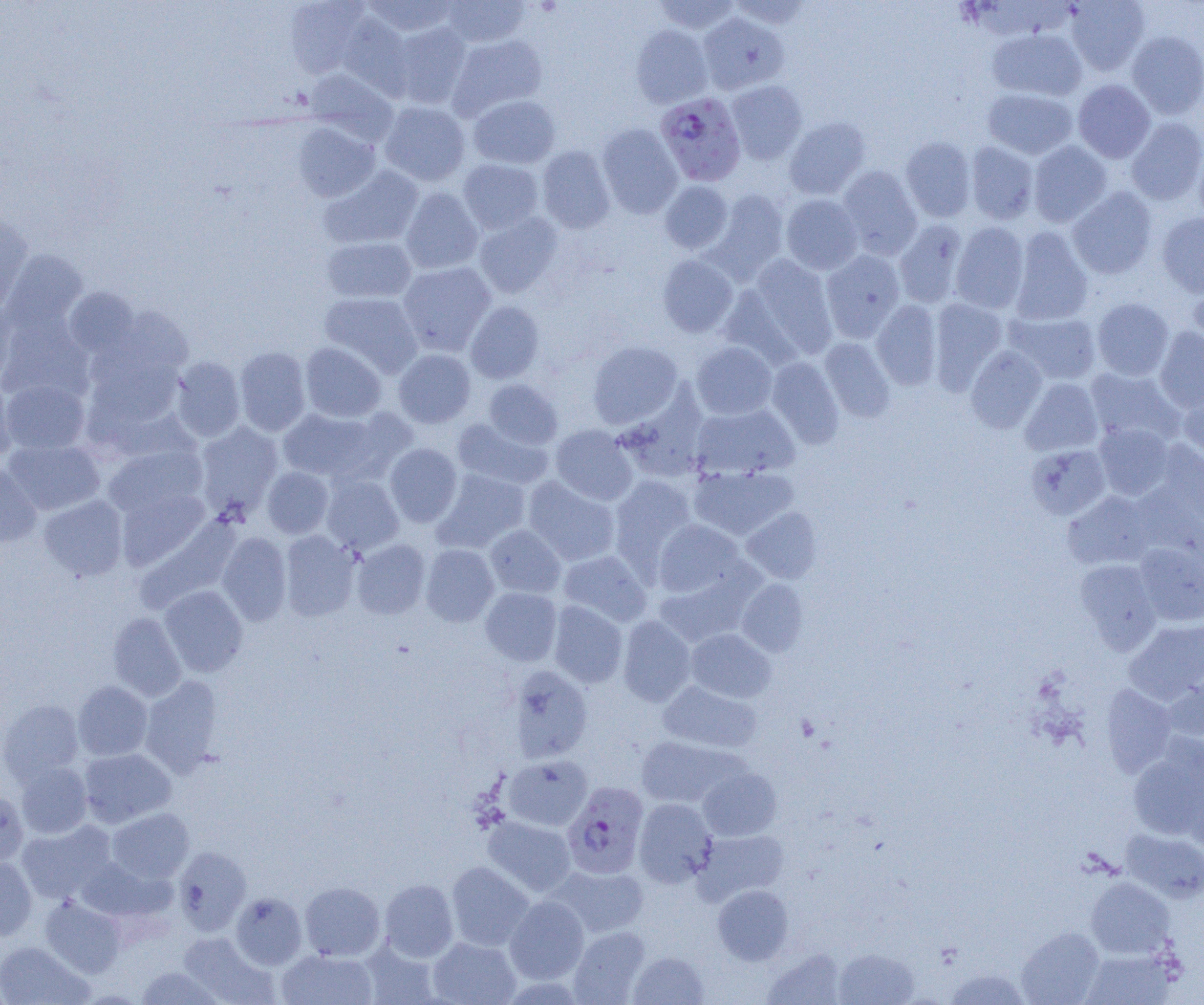

slide-level diagnosis = Plasmodium falciparum
modality = optical microscopy
Plasmodium falciparum-infected red blood cell locations = approximate bounding boxes as (x1,y1)-(x2,y2) corner pairs in pixels: (655,92)-(746,186), (562,782)-(649,879)
uninfected red blood cell locations = approximate bounding boxes as (x1,y1)-(x2,y2) corner pairs in pixels: (284,0)-(374,79), (361,0)-(460,37), (441,0)-(531,48), (653,0)-(740,34), (728,0)-(812,29), (1065,0)-(1150,75), (698,12)-(788,93), (336,13)-(414,98), (389,22)-(472,108), (631,25)-(713,108), (987,28)-(1087,101), (1127,30)-(1204,118), (447,34)-(547,120), (304,68)-(398,143), (726,80)-(807,164), (1073,80)-(1155,163), (982,87)-(1077,159), (469,95)-(561,169), (379,101)-(470,186), (292,112)-(471,191), (784,117)-(871,199), (1126,117)-(1204,205), (292,121)-(380,202), (597,124)-(682,218), (901,136)-(976,222), (966,141)-(1038,224), (1028,141)-(1112,227), (536,145)-(616,233), (1193,147)-(1204,227), (458,158)-(543,234), (319,166)-(424,250), (837,166)-(922,259), (659,181)-(733,254), (400,187)-(483,274), (1068,187)-(1157,279), (706,190)-(789,281), (781,194)-(863,274), (474,212)-(563,298), (1157,212)-(1204,298), (0,215)-(34,316), (895,219)-(968,308), (950,223)-(1029,313), (1010,228)-(1092,325), (322,236)-(417,303), (3,249)-(87,331), (820,250)-(905,341), (657,254)-(738,337), (744,256)-(838,359), (397,261)-(495,355), (1186,284)-(1204,354), (64,287)-(142,360), (320,292)-(423,377), (1092,298)-(1174,380), (929,299)-(1007,392), (872,300)-(942,389), (465,301)-(545,383), (0,302)-(18,388), (108,305)-(194,378), (1006,310)-(1101,384), (0,314)-(95,403), (1154,326)-(1204,412), (819,337)-(895,422), (588,341)-(682,428), (691,342)-(778,420), (300,343)-(386,422), (965,346)-(1046,433), (234,347)-(311,436), (85,349)-(186,432), (393,349)-(476,428), (170,357)-(245,442), (766,358)-(844,448), (1085,368)-(1184,447), (1020,378)-(1103,456), (1,379)-(90,454), (484,379)-(563,449), (0,380)-(17,462), (1178,386)-(1204,463), (616,390)-(712,483), (690,403)-(800,480), (278,407)-(382,483), (452,418)-(553,490), (195,421)-(283,517), (1094,423)-(1174,500), (551,425)-(637,505), (3,440)-(104,515), (1156,440)-(1204,521), (384,443)-(462,527), (1026,444)-(1111,520), (103,445)-(207,520), (0,462)-(41,548), (689,464)-(798,540), (262,467)-(333,538), (433,469)-(530,552), (322,475)-(403,555), (609,475)-(698,573), (523,477)-(620,566), (115,488)-(209,571), (1063,492)-(1156,570), (39,495)-(128,581), (741,507)-(822,583), (136,516)-(242,613), (653,519)-(747,599), (485,524)-(566,598), (279,530)-(360,621), (217,532)-(291,626), (351,539)-(431,619), (1134,542)-(1204,625), (420,544)-(499,626), (559,550)-(651,626), (1075,559)-(1161,653), (736,578)-(808,656), (159,585)-(248,677), (480,587)-(562,666), (548,601)-(628,688), (108,612)-(187,701), (618,615)-(696,707), (1125,619)-(1204,704), (685,629)-(776,703), (507,665)-(593,763), (1162,671)-(1204,743), (139,675)-(224,777), (73,681)-(152,761), (658,681)-(761,753), (1101,685)-(1177,776), (0,698)-(84,784), (635,736)-(743,808), (1128,739)-(1204,841), (79,748)-(176,827), (503,755)-(593,831), (16,762)-(92,839), (698,767)-(781,841), (0,791)-(29,868), (634,798)-(717,887), (107,808)-(194,883), (482,816)-(576,897), (17,820)-(116,904), (694,828)-(789,904), (1121,828)-(1204,903), (173,846)-(251,935), (0,857)-(37,941), (75,857)-(174,926), (446,861)-(535,951), (550,864)-(650,937), (1086,877)-(1174,958), (379,879)-(458,962), (300,881)-(385,961), (713,884)-(793,965), (231,892)-(306,969), (505,895)-(589,984), (40,896)-(126,977), (568,926)-(651,1004), (1016,927)-(1104,1005), (177,932)-(278,1004), (427,936)-(521,1005), (359,940)-(441,1005), (0,941)-(92,1005), (833,947)-(919,1005), (1080,948)-(1178,1005), (276,949)-(378,1005), (761,949)-(847,1004), (628,951)-(709,1005), (135,966)-(224,1004), (942,967)-(1031,1005)
field of view = single
image size = 1204×1005 pixels
magnification = 1000x
preparation = thin blood smear